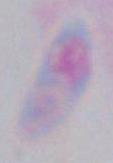

identification = Toxoplasma gondii
modality = micrograph
magnification = 1000x